Assess the morphology of the red blood cells.
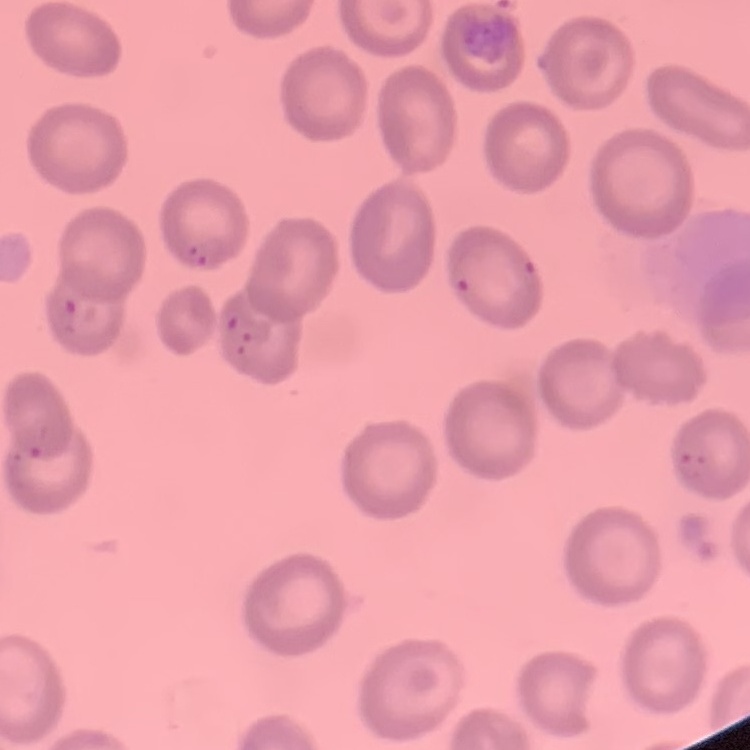

No rouleaux formation.

stain: Field's or Giemsa
image_type: one tile cut from a larger photomicrograph
preparation: thin blood smear